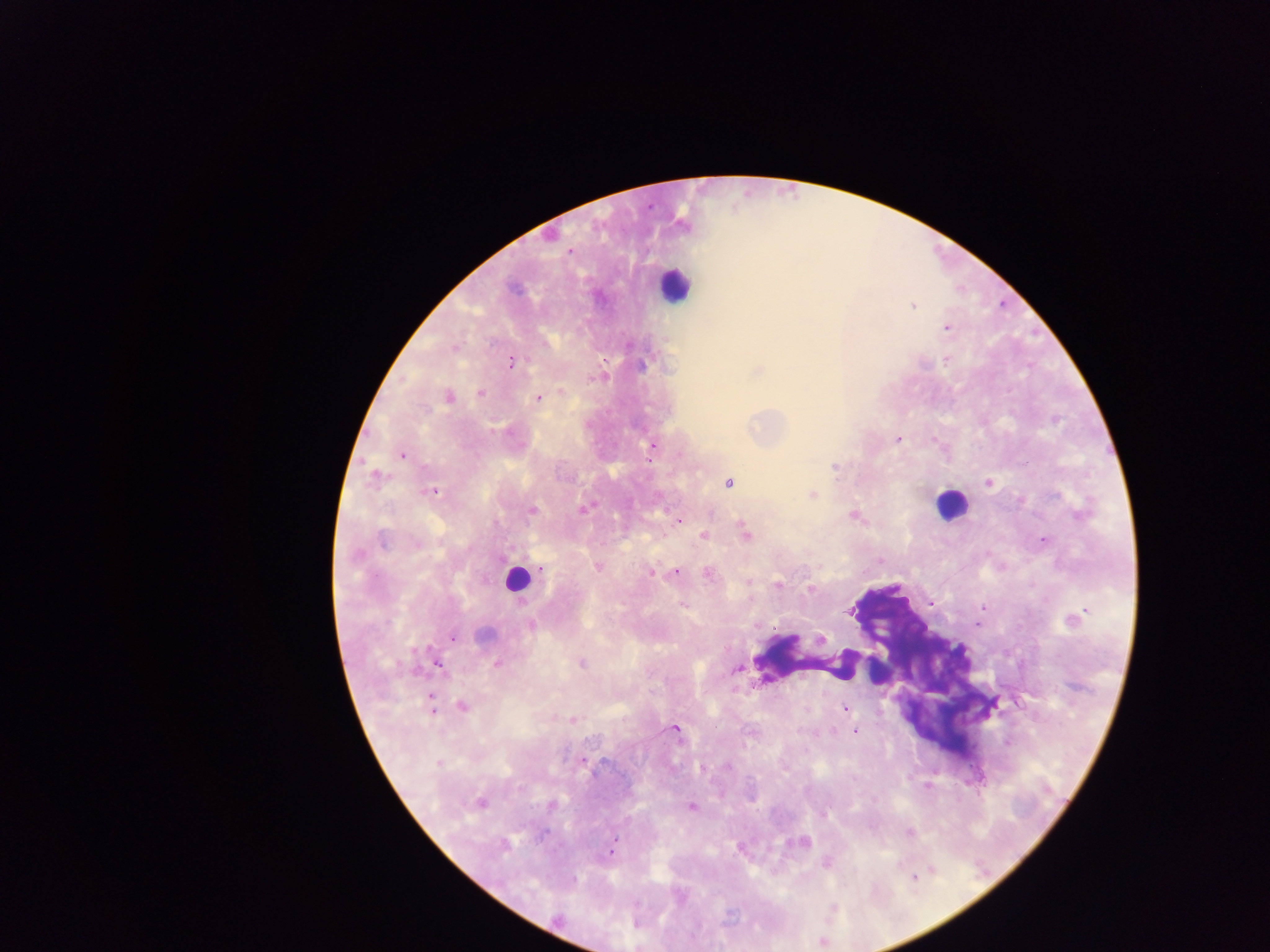
image size = 1270×952 pixels
leukocyte locations = approximate centers as x y in pixels: 674 284; 949 505; 518 578; 811 663
Plasmodium parasite locations = approximate centers as x y in pixels: 570 251; 912 306; 947 327; 454 348; 947 359; 604 361; 511 362; 758 371; 480 393; 448 397; 538 398; 898 439; 653 448; 402 455; 835 467; 375 478; 729 483; 989 483; 431 491; 813 495; 584 509; 532 510; 852 516; 678 521; 745 532; 704 536; 383 540; 1044 540; 417 544; 357 556; 597 566; 541 569; 675 572; 651 573; 708 574; 778 585; 810 589; 682 604; 982 607; 1075 618; 531 625; 484 634; 452 638; 821 639; 497 664; 582 664; 438 666; 737 668; 432 705; 463 706; 843 708; 572 720; 675 729; 855 732; 582 760; 438 763; 701 768; 480 802; 692 807; 823 814; 909 833; 803 842; 504 845; 610 852; 914 878
country = Ghana
capture = mobile-phone photograph through a microscope
field of view = single
preparation = thick blood smear